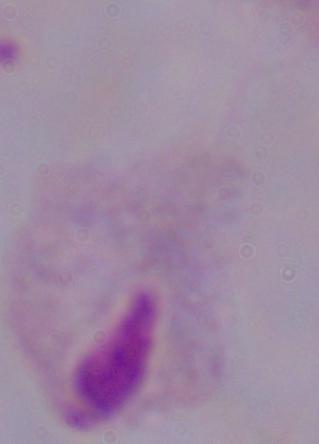
1000x magnification. A trichomonad is seen. Photomicrograph.